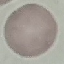
Summary:
  - Malaria status: uninfected
  - Image type: automatically extracted cell patch, resized to 64 × 64 pixels
  - Preparation: thin blood film
  - Stain: Giemsa
  - Capture: smartphone through the microscope eyepiece